Locate and identify every blood parasite.
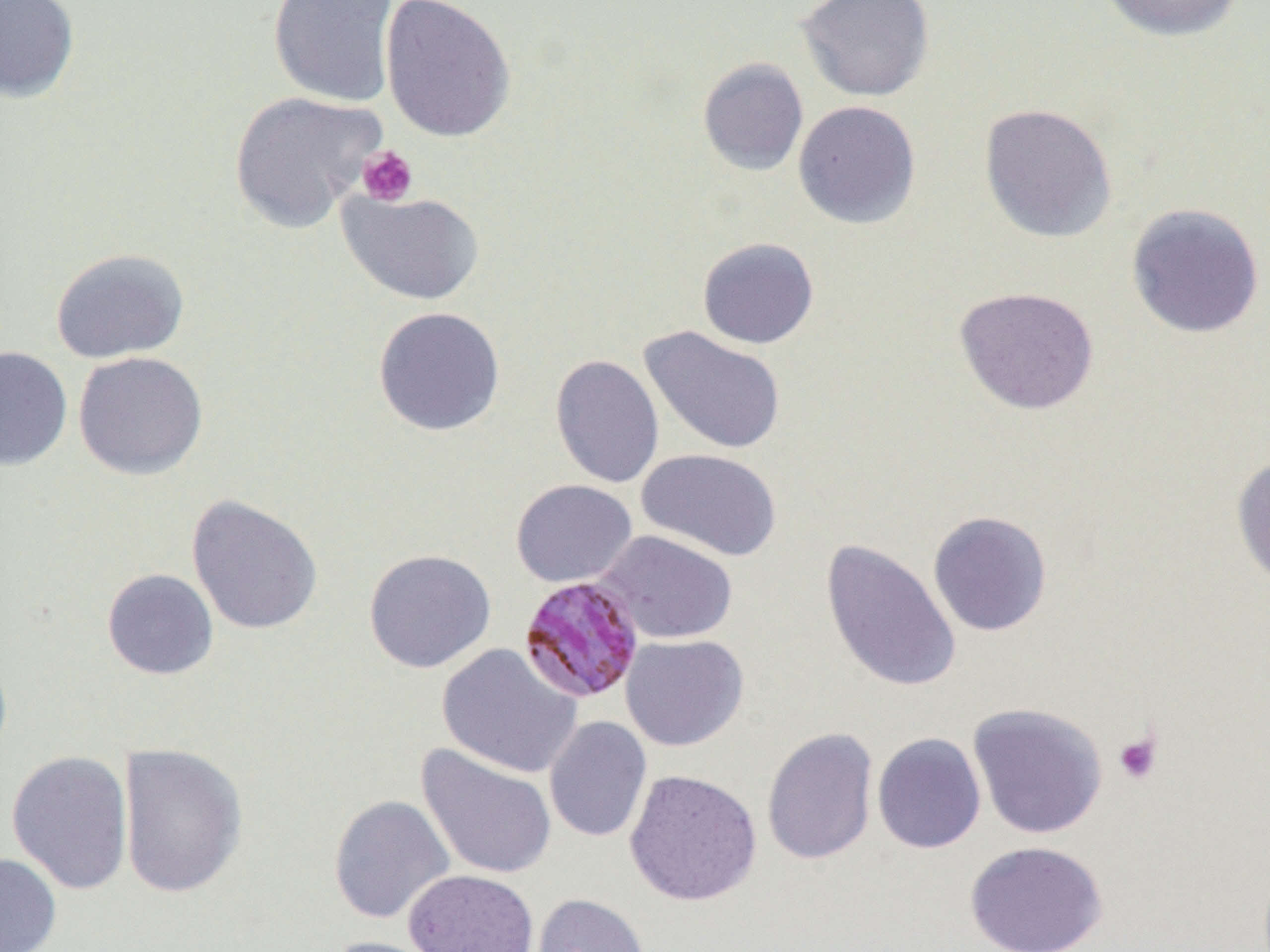
Approximate bounding boxes as [x1, y1, x2, y2] in pixels.
Plasmodium malariae-infected red blood cells: [518, 572, 648, 703].
No Plasmodium falciparum, Plasmodium ovale, Plasmodium vivax, Babesia divergens, or Trypanosoma brucei observed.

Summary:
  - Platelet locations: [357, 145, 419, 206], [1112, 732, 1162, 785]
  - Uninfected red blood cell locations: [0, 0, 80, 103], [268, 0, 399, 108], [380, 0, 516, 142], [795, 0, 935, 101], [1097, 0, 1247, 42], [697, 57, 808, 176], [228, 90, 387, 234], [793, 100, 921, 229], [979, 102, 1118, 243], [336, 188, 485, 306], [1126, 202, 1265, 339], [697, 237, 819, 349], [50, 248, 190, 364], [954, 286, 1099, 415], [373, 306, 506, 436], [638, 326, 787, 456], [0, 346, 72, 471], [72, 352, 208, 480], [550, 354, 664, 488], [636, 448, 782, 562], [1231, 454, 1270, 591], [511, 479, 637, 588], [186, 494, 323, 635], [927, 510, 1053, 636], [593, 530, 738, 644], [821, 538, 961, 693], [364, 549, 496, 673], [102, 568, 219, 679], [621, 634, 748, 751], [437, 643, 582, 779], [967, 703, 1107, 839], [544, 716, 652, 843], [761, 727, 879, 866], [872, 733, 986, 853], [117, 743, 248, 899], [416, 743, 557, 880], [6, 750, 134, 895], [624, 769, 762, 906], [328, 794, 456, 924], [964, 840, 1107, 952], [0, 851, 62, 952], [404, 869, 539, 951], [529, 892, 649, 952], [318, 936, 449, 952]
  - Slide-level diagnosis: Plasmodium malariae
  - Field of view: single
  - Image size: 1270×952 pixels
  - Magnification: 1000x
  - Modality: optical microscopy
  - Preparation: thin blood smear